State the blood parasite species.
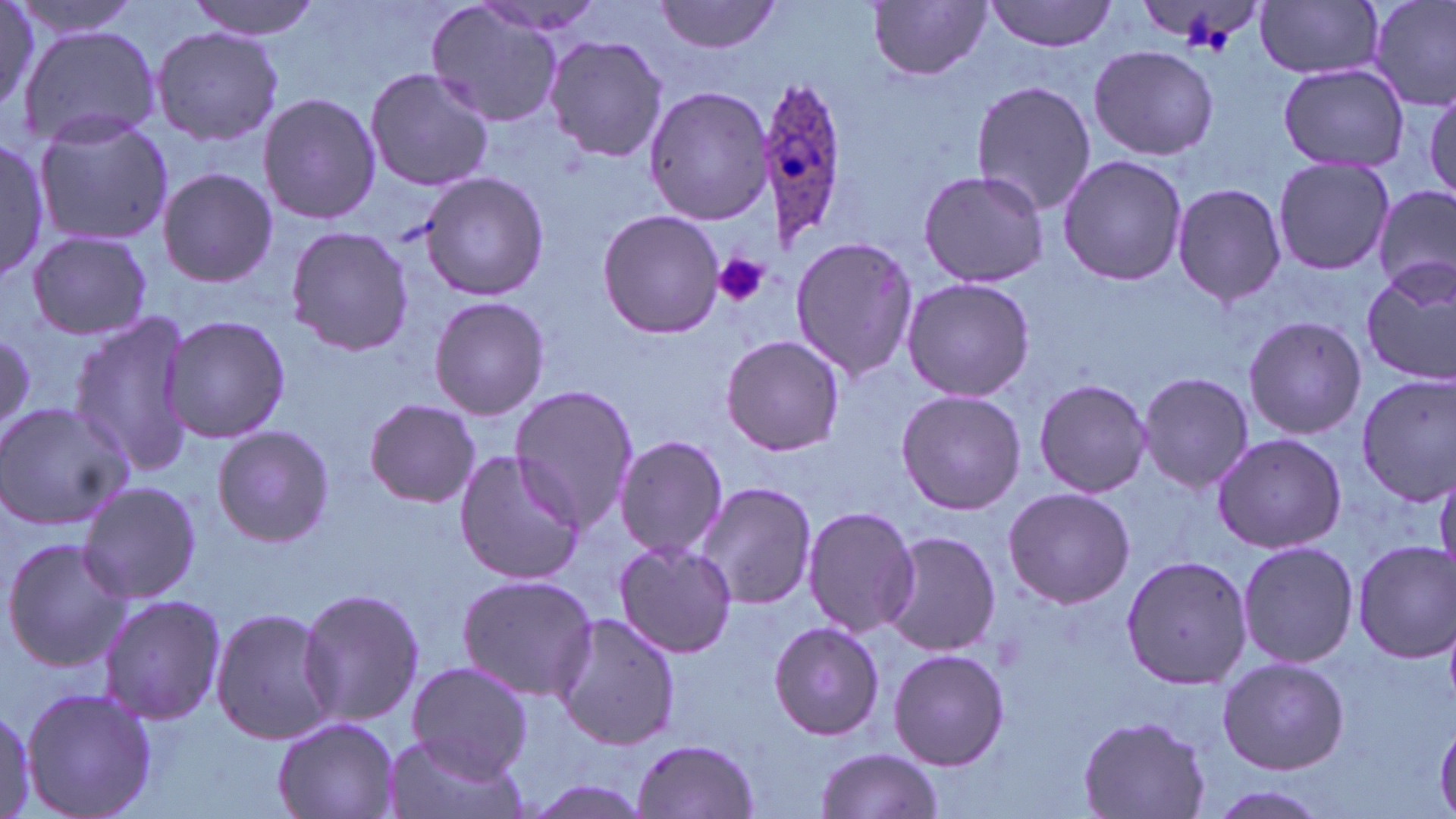

Plasmodium ovale.

{
  "platelet_locations": "approximate bounding boxes as named x1/y1/x2/y2 corners in pixels: (x1=713, y1=253, x2=770, y2=307)",
  "field_of_view": "single",
  "plasmodium_ovale_infected_red_blood_cell_locations": "approximate bounding boxes as named x1/y1/x2/y2 corners in pixels: (x1=755, y1=76, x2=847, y2=248)",
  "image_size": "1456×819 pixels",
  "uninfected_red_blood_cell_locations": "approximate bounding boxes as named x1/y1/x2/y2 corners in pixels: (x1=0, y1=0, x2=56, y2=123), (x1=181, y1=0, x2=324, y2=39), (x1=655, y1=0, x2=781, y2=55), (x1=984, y1=0, x2=1119, y2=52), (x1=1367, y1=0, x2=1456, y2=110), (x1=7, y1=1, x2=149, y2=40), (x1=869, y1=1, x2=989, y2=81), (x1=1256, y1=1, x2=1385, y2=81), (x1=426, y1=3, x2=567, y2=129), (x1=18, y1=23, x2=158, y2=149), (x1=149, y1=27, x2=284, y2=146), (x1=544, y1=33, x2=668, y2=165), (x1=1088, y1=45, x2=1219, y2=162), (x1=1276, y1=64, x2=1411, y2=172), (x1=363, y1=65, x2=495, y2=192), (x1=1424, y1=79, x2=1456, y2=204), (x1=970, y1=80, x2=1098, y2=216), (x1=644, y1=86, x2=773, y2=226), (x1=257, y1=91, x2=381, y2=228), (x1=32, y1=109, x2=174, y2=246), (x1=0, y1=137, x2=50, y2=283), (x1=1055, y1=154, x2=1188, y2=285), (x1=1271, y1=155, x2=1393, y2=277), (x1=155, y1=168, x2=279, y2=290), (x1=418, y1=170, x2=550, y2=302), (x1=916, y1=170, x2=1051, y2=287), (x1=1170, y1=182, x2=1286, y2=309), (x1=1374, y1=185, x2=1455, y2=298), (x1=598, y1=209, x2=725, y2=339), (x1=284, y1=226, x2=414, y2=356), (x1=26, y1=230, x2=152, y2=342), (x1=788, y1=235, x2=918, y2=382), (x1=1358, y1=261, x2=1456, y2=385), (x1=901, y1=277, x2=1035, y2=402), (x1=428, y1=296, x2=552, y2=419), (x1=65, y1=311, x2=196, y2=477), (x1=1243, y1=313, x2=1367, y2=442), (x1=160, y1=314, x2=292, y2=444), (x1=0, y1=328, x2=33, y2=439), (x1=720, y1=334, x2=846, y2=458), (x1=1138, y1=371, x2=1253, y2=495), (x1=1354, y1=373, x2=1456, y2=504), (x1=1031, y1=378, x2=1154, y2=499), (x1=509, y1=386, x2=638, y2=533), (x1=895, y1=389, x2=1026, y2=515), (x1=364, y1=398, x2=480, y2=508), (x1=0, y1=400, x2=132, y2=531), (x1=210, y1=424, x2=335, y2=548), (x1=1211, y1=432, x2=1348, y2=555), (x1=615, y1=433, x2=729, y2=561), (x1=452, y1=451, x2=586, y2=583), (x1=76, y1=479, x2=202, y2=608), (x1=692, y1=481, x2=817, y2=611), (x1=1001, y1=485, x2=1135, y2=607), (x1=806, y1=504, x2=914, y2=640), (x1=880, y1=530, x2=1000, y2=656), (x1=1, y1=536, x2=128, y2=671), (x1=1236, y1=538, x2=1358, y2=670), (x1=612, y1=539, x2=737, y2=659), (x1=1352, y1=539, x2=1454, y2=663), (x1=1120, y1=552, x2=1252, y2=688), (x1=454, y1=573, x2=597, y2=701), (x1=296, y1=587, x2=425, y2=730), (x1=97, y1=594, x2=227, y2=724), (x1=210, y1=606, x2=338, y2=747), (x1=550, y1=610, x2=684, y2=752), (x1=767, y1=620, x2=884, y2=742), (x1=887, y1=648, x2=1011, y2=772), (x1=1215, y1=656, x2=1350, y2=775), (x1=405, y1=662, x2=533, y2=779), (x1=20, y1=684, x2=157, y2=819), (x1=1, y1=702, x2=40, y2=817), (x1=1077, y1=713, x2=1211, y2=818), (x1=272, y1=716, x2=399, y2=819), (x1=386, y1=736, x2=525, y2=819), (x1=631, y1=738, x2=766, y2=819), (x1=813, y1=746, x2=946, y2=819), (x1=519, y1=774, x2=661, y2=819), (x1=1205, y1=784, x2=1335, y2=819)",
  "preparation": "thin blood smear",
  "magnification": "1000x",
  "modality": "light microscopy",
  "stain": "May-Grünwald-Giemsa"
}